Assess this cell for malaria.
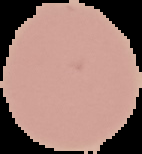

It is uninfected.

{
  "preparation": "thin blood film",
  "image_type": "segmented cell region with the area outside set to black",
  "image_size": "142×154 pixels"
}